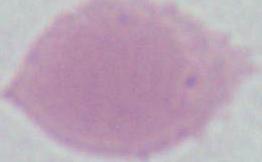
{
  "identification": "erythrocyte",
  "modality": "photomicrograph",
  "magnification": "1000x"
}